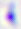
Photomicrograph. Toxoplasma gondii is shown. 400x magnification.